Locate every Plasmodium falciparum parasite and give its life-cycle stage, and locate every leukocyte and any debris.
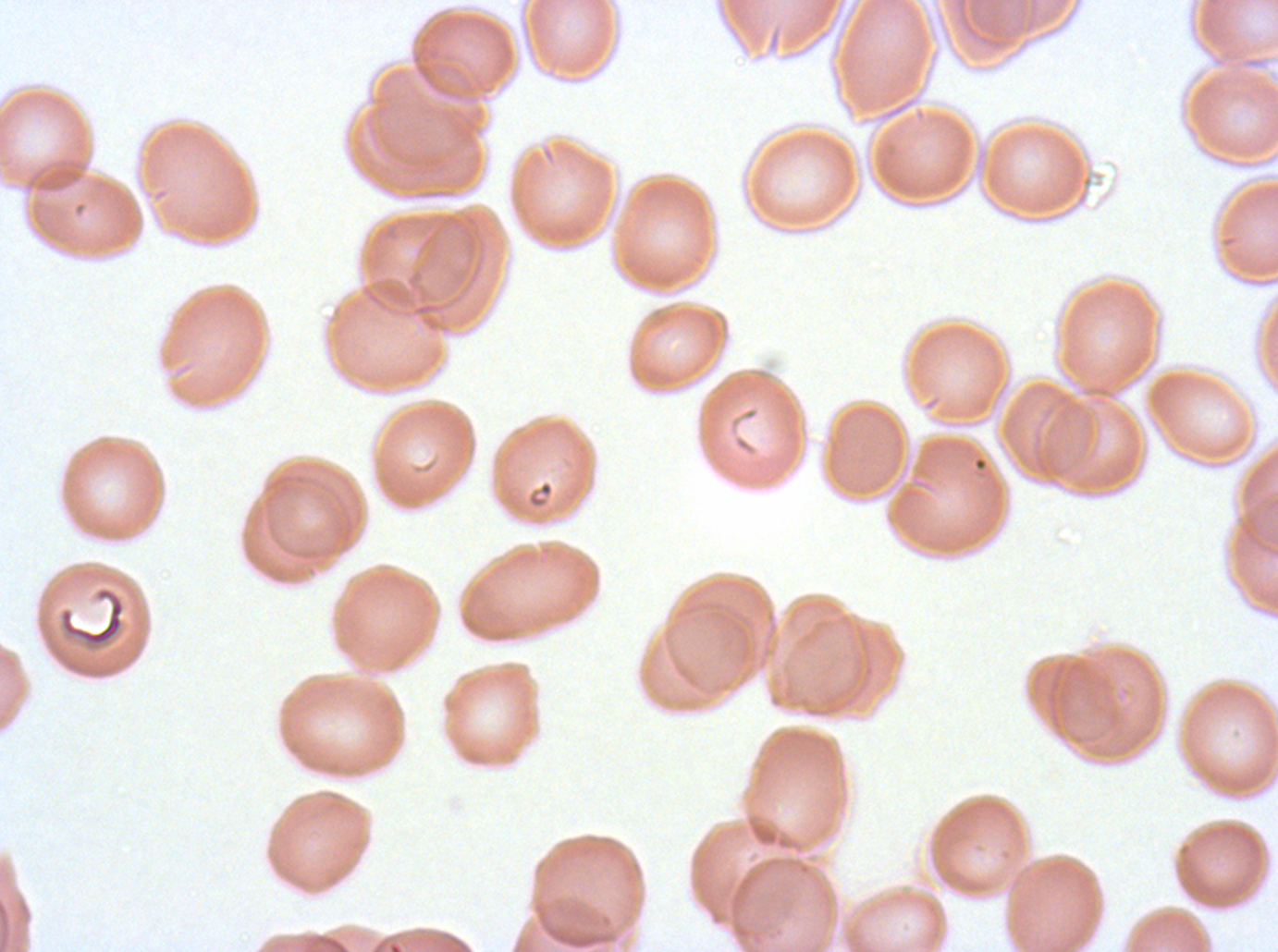

Approximate bounding boxes as (x1, y1, x2, y2) in pixels.
Debris: (58, 586, 126, 652).
No rings, late-ring/early-trophozoite forms, mid trophozoites, late trophozoites, early schizonts, late schizonts, segmenters, gametocytes, or leukocytes observed.

preparation = thin blood film
specimen = ex-vivo Plasmodium falciparum culture from a patient in The Gambia, grown for 24 to 48 hours
image size = 1278×952 pixels
stain = Giemsa
field of view = sub-image separated from a larger composite